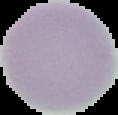

Summary:
  - Result: no malaria parasites detected
  - Preparation: thin blood smear
  - Image type: segmented cell region with the area outside set to black
  - Image size: 118×115 pixels